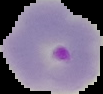
From a thin blood smear. Image is 103×94 pixels. The area outside the segmented cell region is set to black. Result: Plasmodium parasites detected.